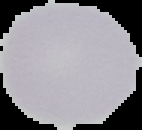

Summary:
  - Malaria status: uninfected
  - Image type: segmented cell region on a black background
  - Preparation: thin blood smear
  - Image size: 142×130 pixels